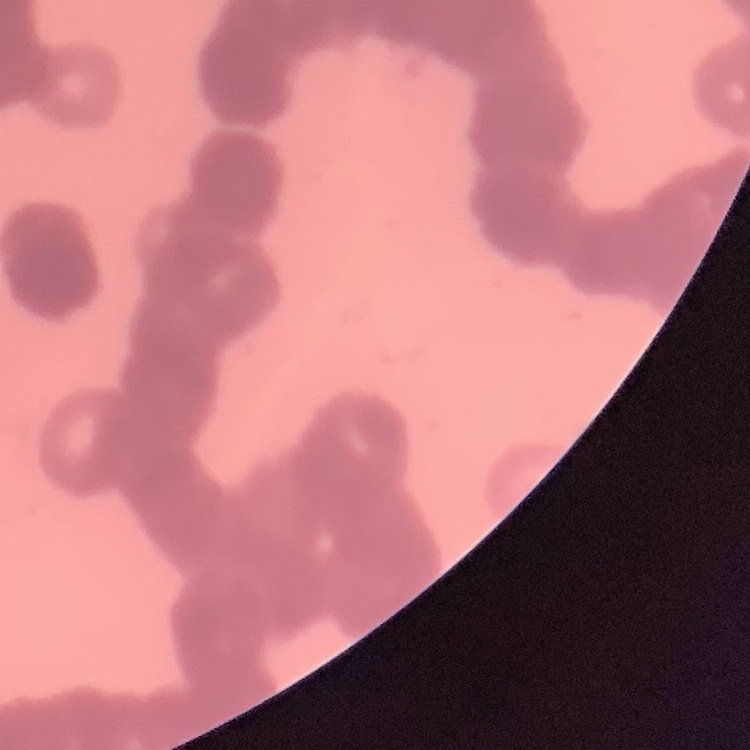
Summary:
  - Erythrocyte morphology: rouleaux formation
  - Image type: one tile cut from a larger photomicrograph
  - Preparation: thin blood film
  - Stain: Field's or Giemsa